State which parasite is depicted.
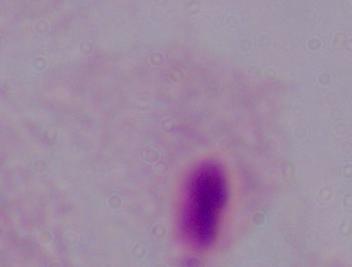

A trichomonad.

Photomicrograph. Captured at 1000x magnification.